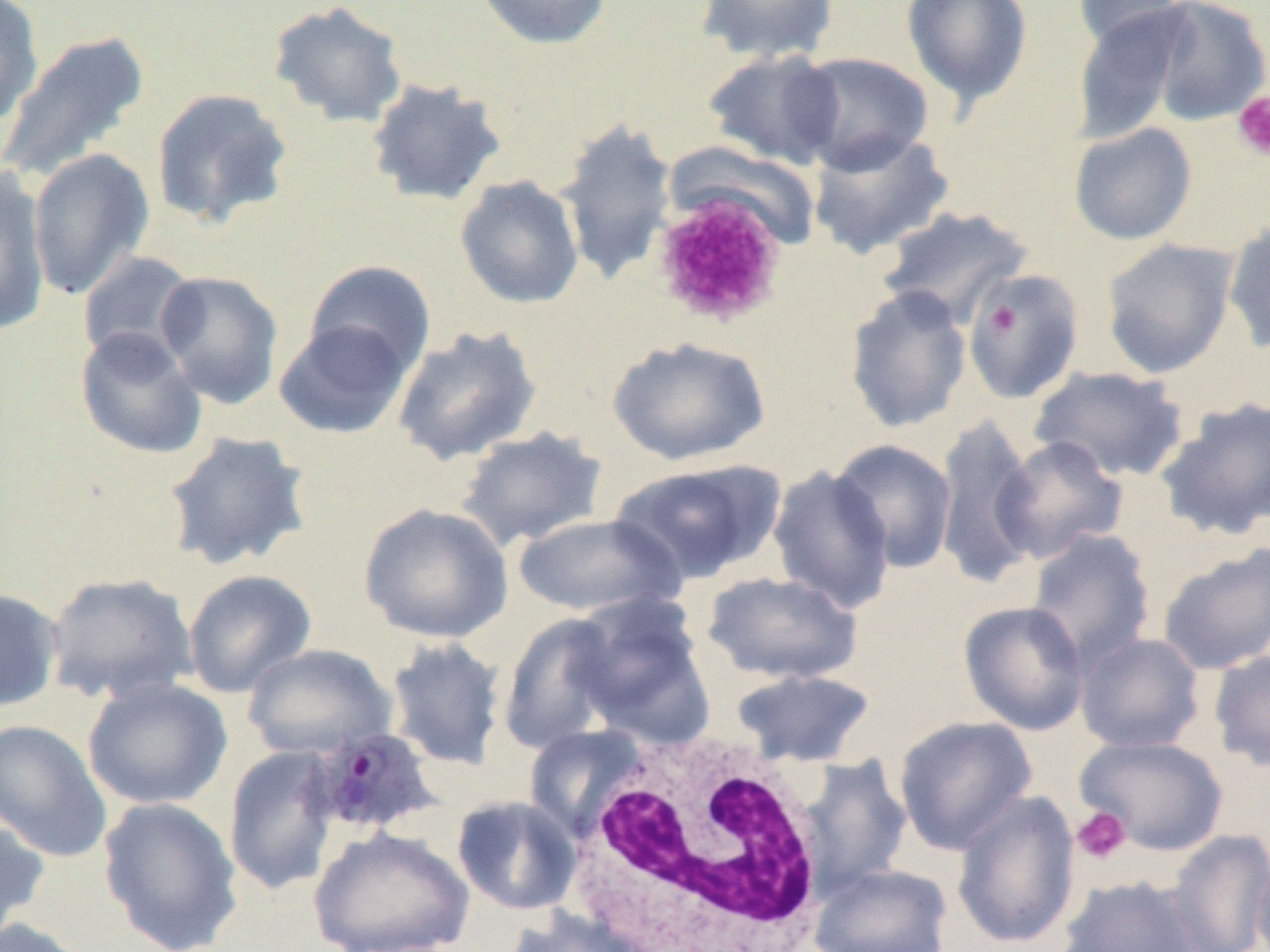

Summary:
  - Coordinate format: approximate bounding boxes as (x1,y1)-(x2,y2) corner pairs in pixels
  - White blood cell locations: (557,728)-(836,951)
  - Plasmodium ovale-infected red blood cell locations: (307,725)-(443,837)
  - Platelet locations: (1232,92)-(1270,162), (987,304)-(1020,336), (1072,806)-(1130,864)
  - Uninfected red blood cell locations: (0,0)-(44,128), (471,0)-(612,50), (696,0)-(839,64), (901,0)-(1033,110), (1145,0)-(1270,126), (267,1)-(409,129), (1071,1)-(1193,52), (1072,5)-(1194,143), (0,30)-(150,186), (701,49)-(846,169), (790,52)-(934,174), (365,78)-(509,207), (151,87)-(294,230), (555,116)-(679,286), (1067,122)-(1197,246), (807,129)-(955,260), (27,149)-(155,299), (0,167)-(52,338), (454,175)-(584,309), (650,190)-(788,326), (876,205)-(1035,329), (1222,218)-(1270,356), (1101,238)-(1240,379), (77,250)-(200,366), (304,260)-(437,378), (155,269)-(284,408), (962,269)-(1086,404), (844,285)-(973,434), (274,319)-(413,440), (390,324)-(542,467), (75,326)-(207,459), (606,335)-(771,466), (1029,365)-(1189,484), (1155,396)-(1270,541), (931,416)-(1041,587), (454,426)-(609,552), (163,430)-(313,572), (992,435)-(1129,565), (829,439)-(958,574), (610,458)-(784,585), (767,465)-(896,614), (358,502)-(514,644), (512,512)-(683,618), (1025,528)-(1157,672), (1157,543)-(1270,675), (182,569)-(317,698), (45,571)-(198,706), (701,571)-(863,685), (0,587)-(64,713), (567,593)-(716,749), (959,600)-(1090,735), (497,613)-(626,754), (1074,632)-(1206,753), (385,636)-(508,771), (242,643)-(397,761), (1209,649)-(1270,772), (729,668)-(877,767), (82,677)-(233,810), (893,716)-(1038,855), (0,719)-(114,863), (1074,734)-(1229,856), (223,745)-(341,897), (799,755)-(913,896), (951,789)-(1081,951), (450,794)-(582,916), (97,796)-(244,952), (0,816)-(51,942), (309,827)-(474,952), (1167,829)-(1270,952), (1252,856)-(1270,952), (810,864)-(954,952), (1056,874)-(1204,952), (504,908)-(651,952), (0,917)-(92,952)
  - Slide-level diagnosis: Plasmodium ovale
  - Field of view: single
  - Preparation: thin blood film
  - Modality: optical microscopy
  - Magnification: 1000x
  - Image size: 1270×952 pixels